Name the parasite shown.
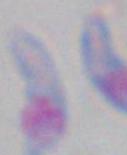

This is Toxoplasma gondii.

{
  "magnification": "1000x",
  "modality": "photomicrograph"
}